Give the extent of all uninfected red blood cells.
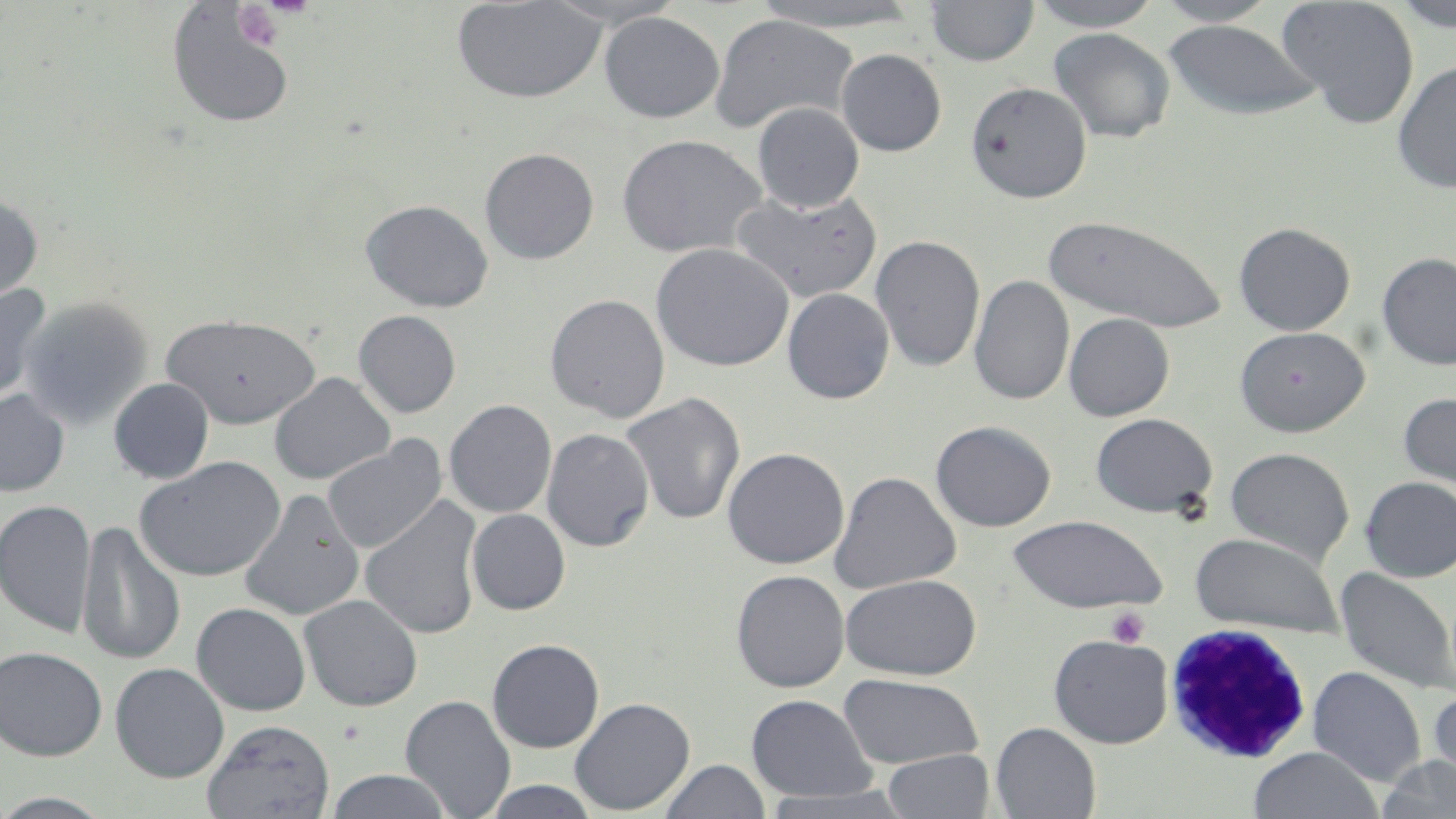

Approximate bounding boxes as (x1, y1, x2, y2) in pixels.
Uninfected red blood cells: (451, 0, 608, 104), (1027, 0, 1163, 31), (1152, 0, 1282, 26), (1277, 0, 1420, 128), (1390, 0, 1456, 33), (925, 1, 1039, 68), (165, 2, 297, 129), (751, 2, 923, 33), (598, 11, 725, 123), (709, 13, 860, 135), (1162, 19, 1322, 120), (1048, 27, 1175, 144), (835, 48, 947, 157), (1392, 60, 1456, 194), (965, 80, 1093, 202), (752, 103, 864, 213), (616, 133, 769, 260), (480, 148, 599, 264), (730, 189, 881, 302), (0, 191, 43, 305), (361, 199, 493, 312), (1042, 215, 1229, 334), (1233, 221, 1356, 336), (870, 234, 985, 373), (651, 242, 794, 372), (1377, 251, 1456, 371), (969, 274, 1074, 406), (0, 282, 51, 404), (782, 288, 895, 404), (544, 294, 670, 422), (20, 296, 153, 430), (353, 310, 461, 418), (1063, 313, 1174, 421), (161, 314, 321, 428), (1234, 326, 1369, 436), (270, 373, 395, 485), (109, 378, 214, 484), (0, 389, 69, 496), (1397, 392, 1456, 494), (621, 393, 746, 526), (444, 399, 557, 518), (1090, 412, 1218, 517), (930, 420, 1056, 532), (541, 427, 654, 552), (322, 438, 446, 554), (722, 446, 849, 569), (1224, 447, 1354, 566), (134, 457, 286, 581), (829, 470, 961, 594), (1360, 475, 1456, 582), (239, 489, 365, 621), (360, 495, 484, 640), (0, 500, 96, 637), (467, 509, 570, 615), (1006, 514, 1167, 614), (77, 519, 186, 667), (1189, 532, 1344, 636), (1335, 567, 1456, 697), (731, 570, 850, 692), (840, 574, 982, 680), (299, 595, 423, 711), (191, 602, 311, 716), (1048, 634, 1173, 748), (487, 638, 604, 753), (0, 645, 108, 761), (110, 662, 230, 783), (1308, 665, 1426, 787), (838, 673, 984, 769), (1426, 686, 1456, 799), (400, 694, 517, 818), (746, 694, 877, 803), (569, 696, 695, 815), (201, 719, 336, 819), (991, 722, 1101, 819), (1247, 747, 1384, 819), (881, 749, 996, 818), (1377, 756, 1456, 818), (660, 760, 769, 818), (325, 769, 454, 819), (478, 780, 603, 818), (758, 786, 917, 818), (0, 791, 118, 818).

{
  "slide_level_diagnosis": "Plasmodium malariae",
  "platelet_locations": "approximate bounding boxes as (x1, y1, x2, y2) in pixels: (233, 4, 282, 50), (1105, 607, 1149, 648)",
  "field_of_view": "one of a larger specimen",
  "magnification": "1000x",
  "stain": "May-Grünwald-Giemsa",
  "white_blood_cell_locations": "approximate bounding boxes as (x1, y1, x2, y2) in pixels: (1164, 624, 1314, 765)",
  "modality": "optical microscopy",
  "preparation": "thin blood smear",
  "image_size": "1456×819 pixels"
}